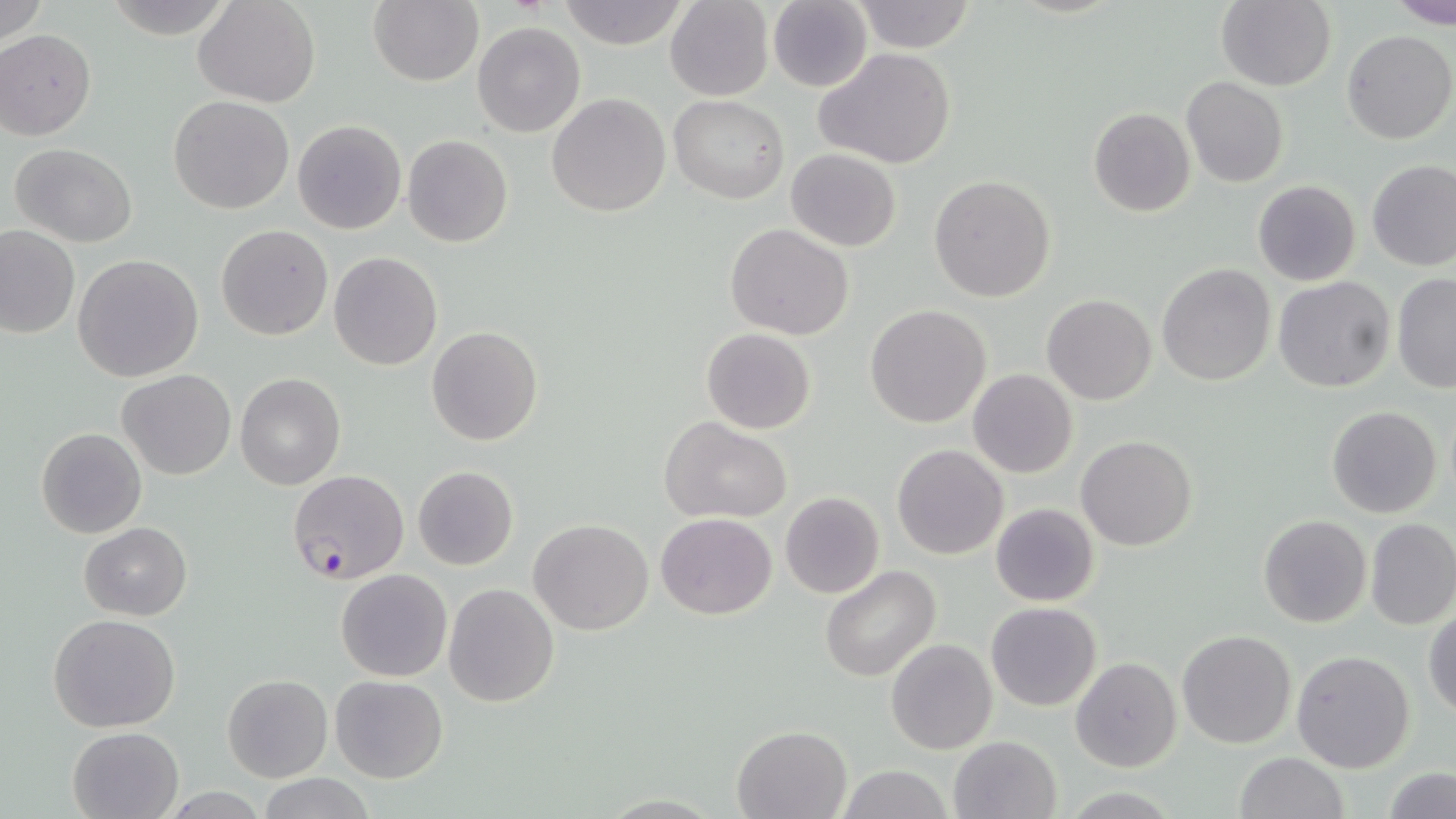 Approximate bounding boxes as (x1,y1)-(x2,y2) corner pairs in pixels. Plasmodium falciparum-infected red blood cell locations: (288,468)-(409,585). Uninfected red blood cell locations: (0,0)-(48,48), (195,0)-(321,108), (369,0)-(483,86), (558,0)-(691,49), (853,0)-(977,53), (1215,0)-(1335,90), (1388,0)-(1456,27), (665,1)-(773,101), (767,2)-(872,91), (472,22)-(585,137), (1341,29)-(1456,145), (0,30)-(97,140), (816,49)-(957,169), (1181,77)-(1288,187), (547,93)-(672,218), (669,95)-(790,203), (167,96)-(295,215), (1087,107)-(1196,217), (292,120)-(406,235), (402,134)-(513,248), (9,142)-(139,248), (786,148)-(901,252), (1367,161)-(1456,271), (929,175)-(1056,302), (1252,179)-(1361,286), (216,223)-(333,341), (724,223)-(854,340), (0,224)-(80,338), (328,251)-(443,370), (73,254)-(204,382), (1156,263)-(1275,386), (1391,273)-(1455,393), (1273,276)-(1396,393), (1042,294)-(1157,405), (865,304)-(992,429), (426,326)-(543,446), (701,328)-(816,434), (117,369)-(236,479), (968,369)-(1077,478), (236,373)-(345,490), (1326,404)-(1443,518), (660,415)-(792,523), (36,427)-(146,538), (1075,435)-(1198,549), (892,444)-(1008,561), (412,466)-(519,569), (779,491)-(885,599), (989,504)-(1100,607), (655,513)-(776,620), (1258,514)-(1371,628), (528,519)-(655,636), (1365,519)-(1456,630), (78,522)-(192,620), (819,564)-(942,681), (336,568)-(452,681), (444,583)-(560,706), (986,601)-(1102,711), (1424,610)-(1456,716), (49,614)-(182,733), (1177,629)-(1295,749), (886,638)-(997,755), (1291,650)-(1416,773), (1070,656)-(1182,771), (222,674)-(333,783), (330,674)-(448,783), (732,724)-(852,818), (67,727)-(184,819), (950,735)-(1062,818), (1233,752)-(1348,819), (832,765)-(956,819), (1383,767)-(1456,819), (258,773)-(375,819). Slide-level diagnosis: Plasmodium falciparum. Light microscopy. 1000x magnification. Single field of view. May-Grünwald-Giemsa-stained preparation. Thin blood smear. Image is 1456×819 pixels.